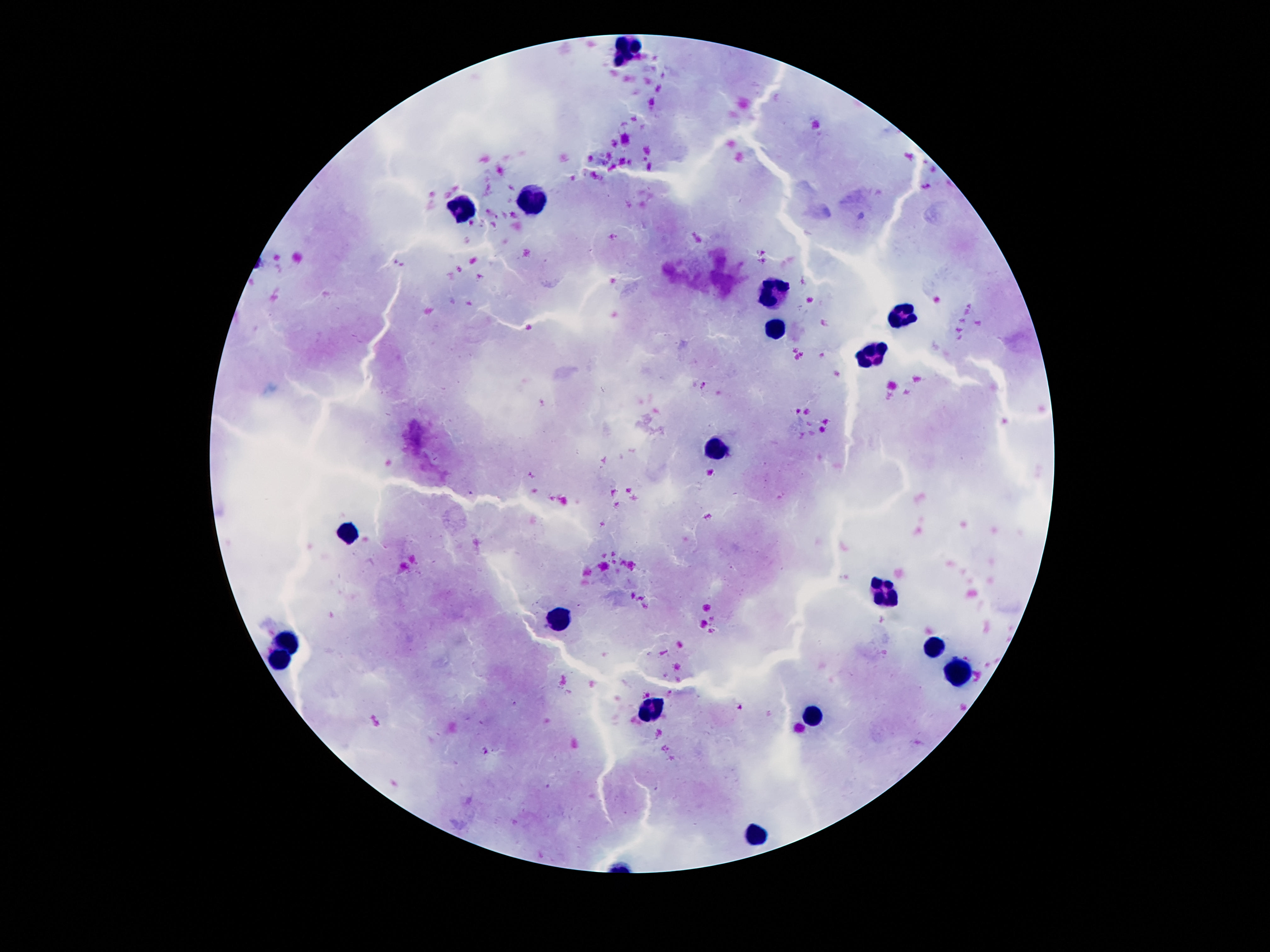
Approximate centers as (x, y) in pixels. Leukocyte locations: (628, 46), (532, 199), (461, 210), (772, 287), (902, 319), (770, 327), (870, 358), (716, 447), (346, 532), (884, 594), (558, 619), (289, 641), (936, 651), (279, 660), (962, 672), (652, 710), (810, 716), (758, 830). Giemsa-stained preparation. One field from this slide. Image is 1270×952 pixels. Patient malaria status: negative. 100x magnification. Thick blood smear. Photographed through the microscope eyepiece with a smartphone camera.